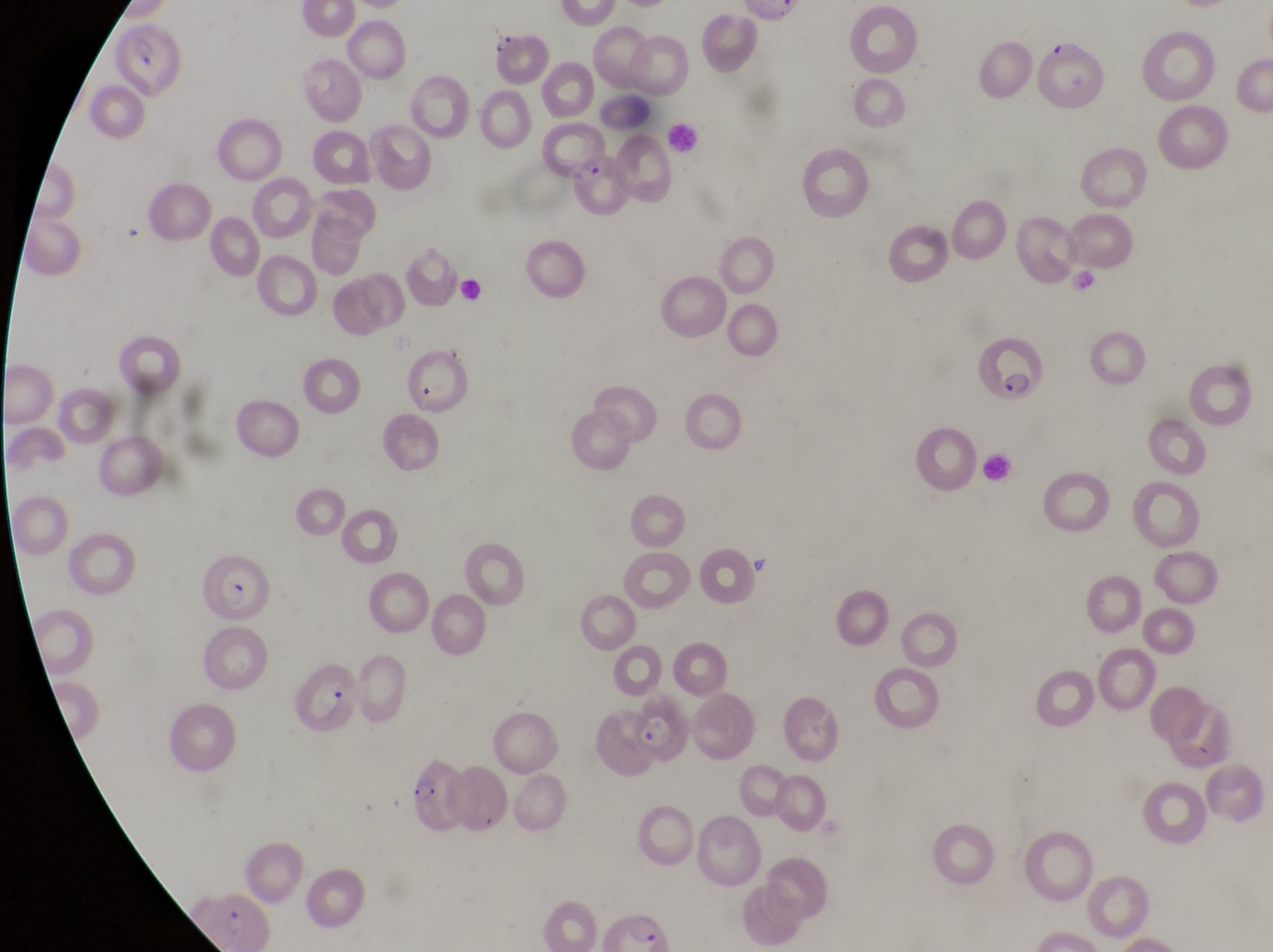

Approximate bounding boxes as [left, top, right, bottom] in pixels.
Summary:
  - Leukocyte locations: [663, 116, 704, 153]
  - Parasitised red blood cell locations: [120, 23, 185, 100], [567, 154, 629, 217], [978, 330, 1053, 407], [200, 556, 278, 628], [295, 659, 360, 736], [621, 711, 693, 768], [404, 756, 467, 831]
  - Artifact (platelet-like body, stain precipitate, or debris) locations: [487, 23, 515, 58]
  - Image size: 1273×952 pixels
  - Country: Uganda
  - Magnification: 1000x
  - Preparation: thin blood smear
  - Field of view: single
  - Capture: smartphone photograph through the eyepiece of an Olympus CX-23 microscope